Classify this cell by malaria status.
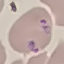

Parasitized.

preparation = thin smear
image type = cell patch, automatically extracted from a larger field of view and resized to 64 × 64 pixels
stain = Giemsa
capture = smartphone camera at the microscope eyepiece